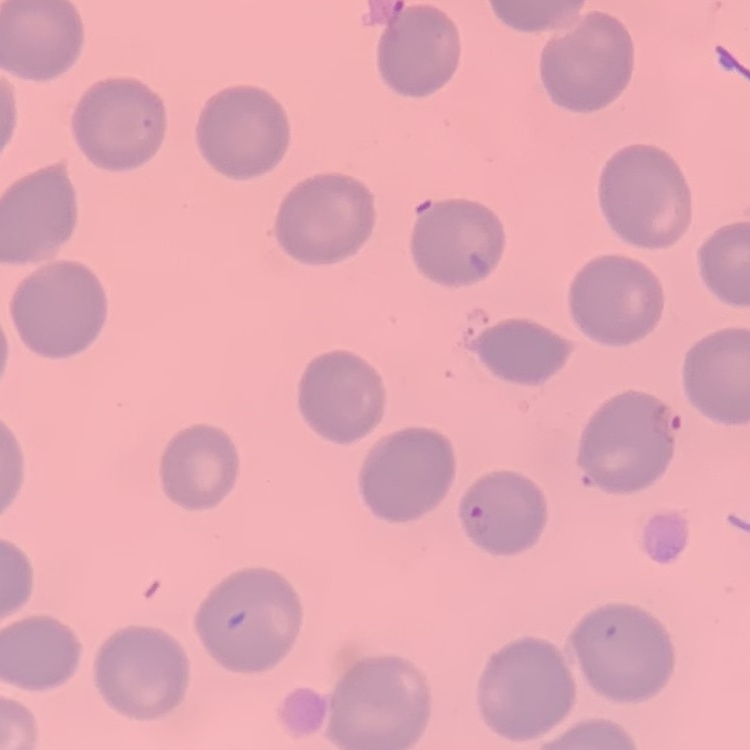
red_blood_cell_morphology: no rouleaux formation
image_type: square crop of a larger photomicrograph
preparation: thin blood smear
stain: Field's or Giemsa